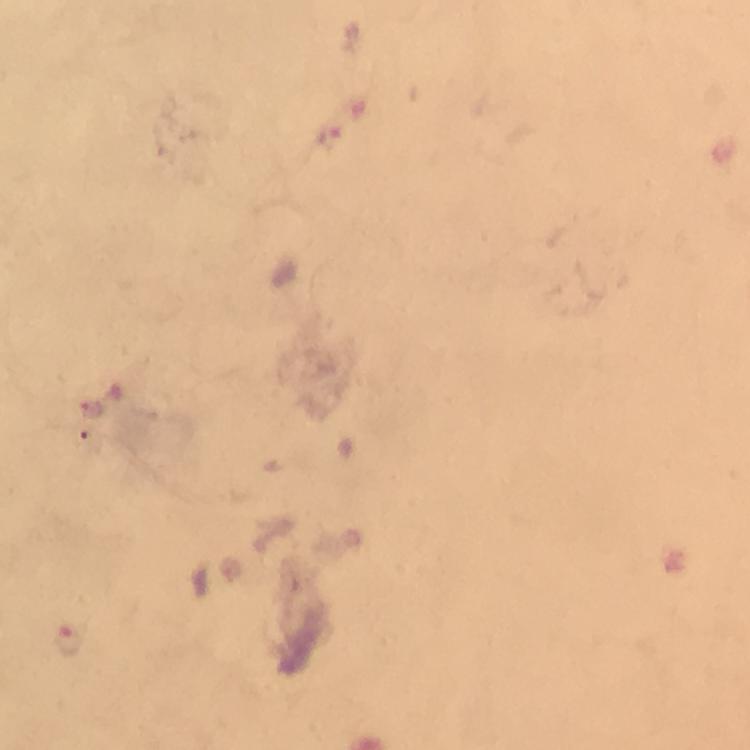

Approximate centers as {x, y} in pixels. Malaria parasite locations: {327, 131}, {92, 409}, {68, 639}. Photographed through the microscope with a smartphone camera. At 100x magnification. From a diagnostic examination for malaria. Image is 750×750 pixels. Giemsa stain. Immersion oil was used. Cropped region of a single field of view. Thick smear.